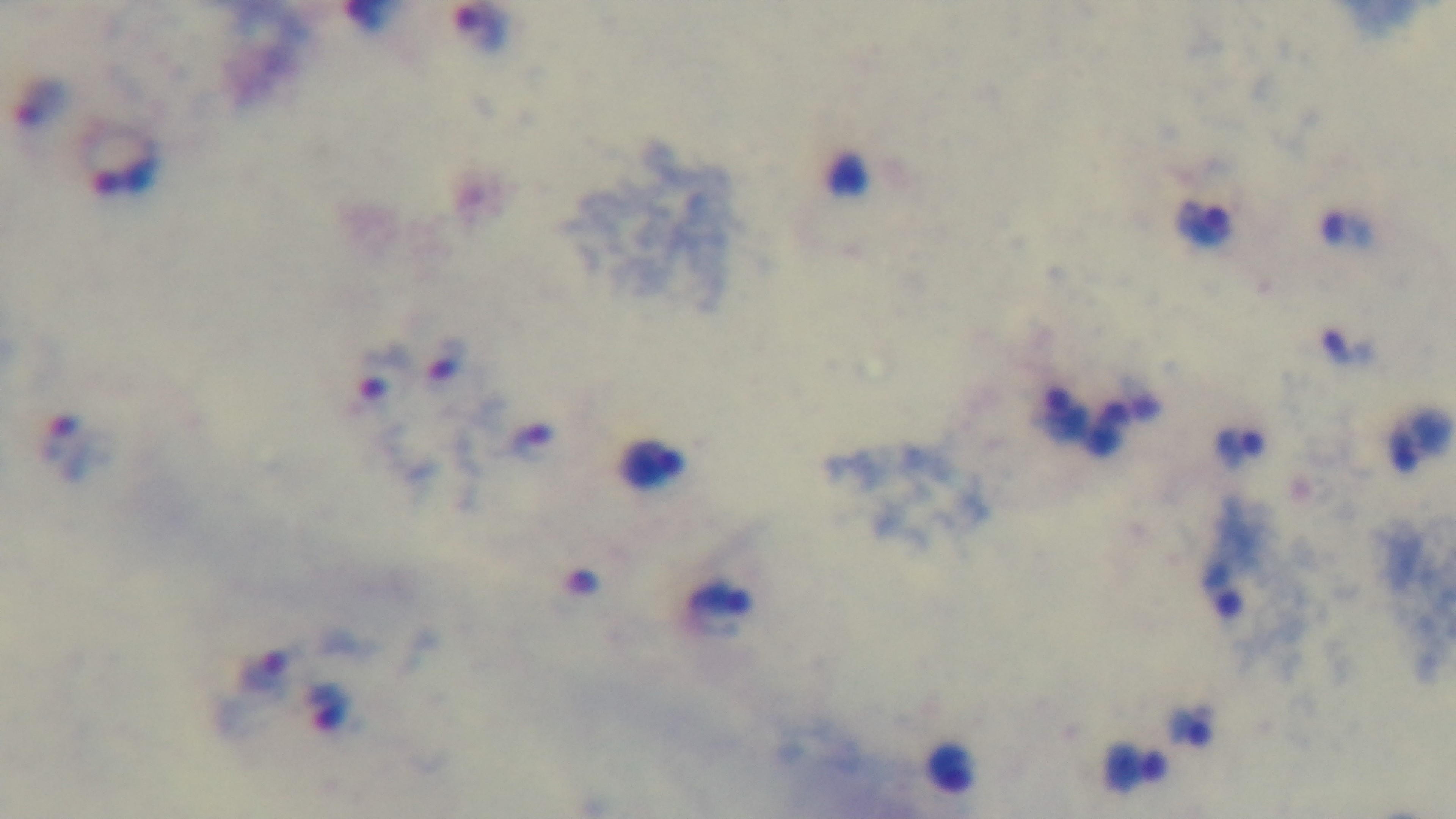
capture = mounted 4K digital camera
modality = light microscopy
malaria status = positive
preparation = thick blood film
objective = 100x oil immersion
stain = Giemsa
field of view = single